Identify the parasite.
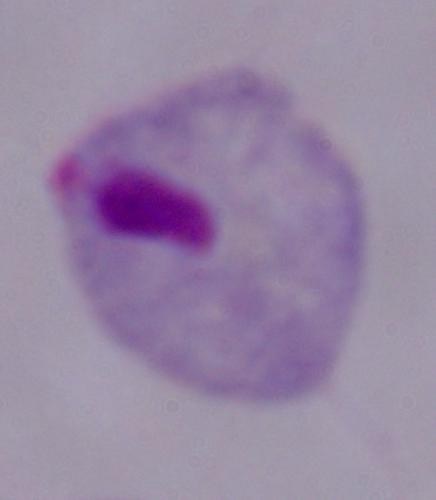
This is a trichomonad.

Captured at 1000x magnification. Micrograph.